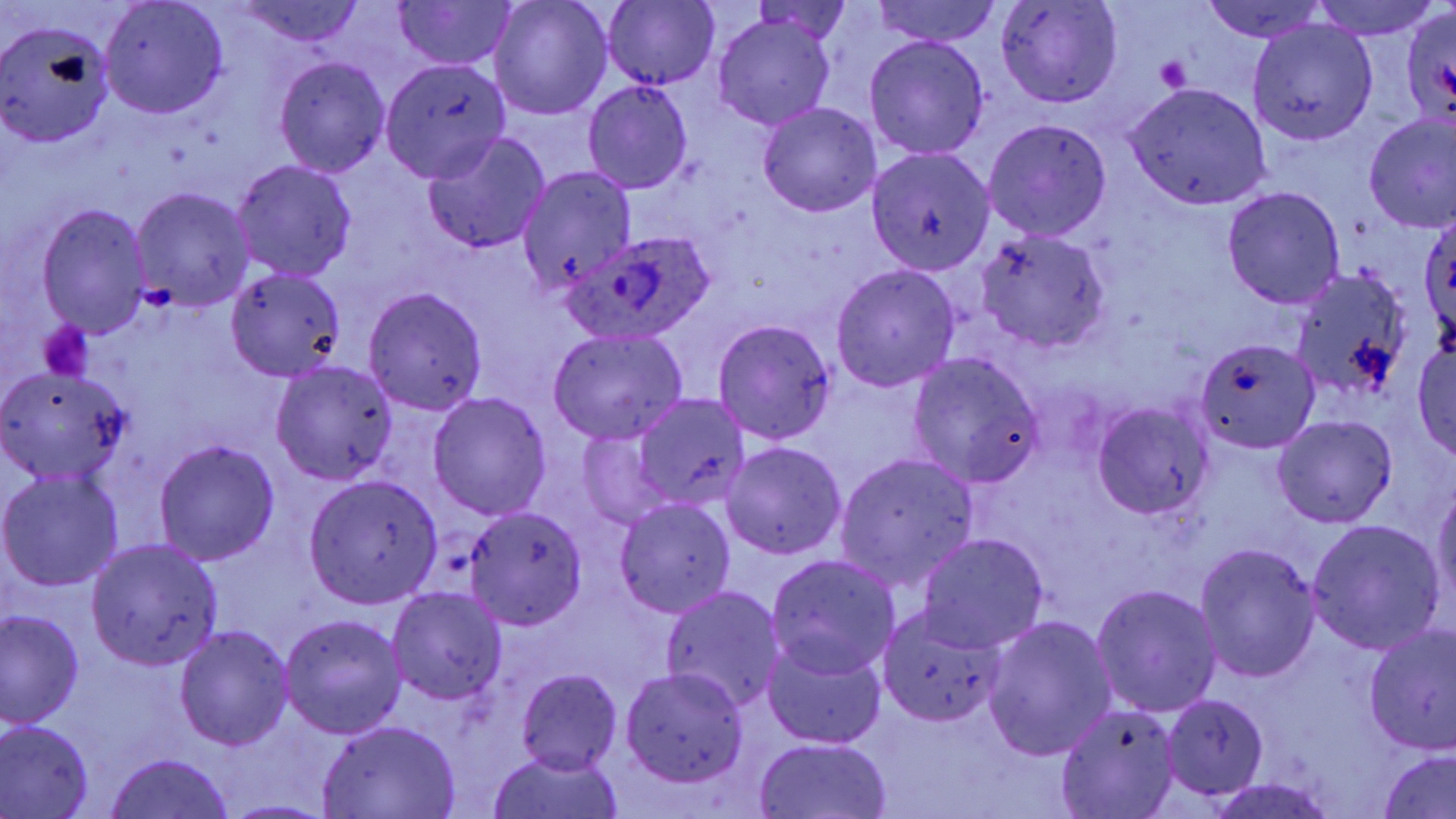

slide-level diagnosis = Plasmodium ovale
magnification = 1000x
image size = 1456×819 pixels
Plasmodium ovale-infected red blood cell locations = approximate bounding boxes as named x1/y1/x2/y2 corners in pixels: (x1=559, y1=232, x2=717, y2=345)
preparation = thin blood smear
uninfected red blood cell locations = approximate bounding boxes as named x1/y1/x2/y2 corners in pixels: (x1=100, y1=0, x2=229, y2=119), (x1=236, y1=0, x2=369, y2=48), (x1=391, y1=0, x2=516, y2=71), (x1=872, y1=0, x2=1003, y2=48), (x1=1203, y1=0, x2=1327, y2=42), (x1=1309, y1=0, x2=1441, y2=39), (x1=488, y1=1, x2=614, y2=120), (x1=749, y1=1, x2=856, y2=45), (x1=994, y1=1, x2=1124, y2=108), (x1=602, y1=2, x2=719, y2=89), (x1=1397, y1=9, x2=1456, y2=128), (x1=713, y1=14, x2=835, y2=130), (x1=0, y1=19, x2=114, y2=147), (x1=1248, y1=19, x2=1378, y2=144), (x1=864, y1=35, x2=990, y2=160), (x1=273, y1=55, x2=391, y2=177), (x1=379, y1=59, x2=513, y2=183), (x1=582, y1=79, x2=693, y2=194), (x1=1124, y1=83, x2=1270, y2=209), (x1=757, y1=102, x2=882, y2=217), (x1=1363, y1=113, x2=1456, y2=234), (x1=983, y1=118, x2=1112, y2=239), (x1=420, y1=132, x2=551, y2=255), (x1=866, y1=147, x2=997, y2=274), (x1=231, y1=159, x2=357, y2=282), (x1=518, y1=166, x2=637, y2=298), (x1=1221, y1=186, x2=1346, y2=309), (x1=130, y1=187, x2=255, y2=310), (x1=35, y1=203, x2=152, y2=338), (x1=1419, y1=208, x2=1456, y2=348), (x1=977, y1=231, x2=1112, y2=353), (x1=831, y1=264, x2=960, y2=392), (x1=225, y1=266, x2=348, y2=380), (x1=1289, y1=268, x2=1419, y2=407), (x1=362, y1=285, x2=490, y2=415), (x1=713, y1=320, x2=836, y2=444), (x1=549, y1=327, x2=688, y2=444), (x1=1194, y1=338, x2=1318, y2=452), (x1=1414, y1=339, x2=1455, y2=462), (x1=907, y1=353, x2=1044, y2=487), (x1=269, y1=361, x2=397, y2=485), (x1=0, y1=364, x2=134, y2=485), (x1=430, y1=392, x2=551, y2=519), (x1=633, y1=395, x2=750, y2=511), (x1=1093, y1=401, x2=1216, y2=520), (x1=1273, y1=415, x2=1396, y2=527), (x1=577, y1=430, x2=669, y2=529), (x1=155, y1=439, x2=279, y2=565), (x1=721, y1=441, x2=847, y2=560), (x1=835, y1=452, x2=978, y2=590), (x1=1, y1=470, x2=124, y2=592), (x1=304, y1=475, x2=443, y2=607), (x1=1431, y1=481, x2=1456, y2=618), (x1=615, y1=498, x2=736, y2=618), (x1=463, y1=506, x2=587, y2=629), (x1=1305, y1=519, x2=1445, y2=655), (x1=916, y1=534, x2=1050, y2=653), (x1=86, y1=538, x2=222, y2=670), (x1=1194, y1=543, x2=1321, y2=683), (x1=765, y1=554, x2=900, y2=681), (x1=1091, y1=583, x2=1222, y2=718), (x1=661, y1=585, x2=785, y2=712), (x1=387, y1=587, x2=508, y2=706), (x1=1, y1=610, x2=83, y2=728), (x1=877, y1=610, x2=1007, y2=730), (x1=278, y1=613, x2=407, y2=739), (x1=981, y1=615, x2=1116, y2=763), (x1=174, y1=626, x2=294, y2=751), (x1=1362, y1=626, x2=1456, y2=757), (x1=762, y1=638, x2=889, y2=751), (x1=619, y1=667, x2=751, y2=787), (x1=516, y1=668, x2=622, y2=775), (x1=1162, y1=694, x2=1267, y2=797), (x1=1055, y1=702, x2=1181, y2=818), (x1=0, y1=720, x2=95, y2=817), (x1=317, y1=720, x2=461, y2=818), (x1=754, y1=738, x2=893, y2=818), (x1=486, y1=748, x2=625, y2=819), (x1=1378, y1=749, x2=1456, y2=818), (x1=104, y1=752, x2=237, y2=819), (x1=1208, y1=778, x2=1338, y2=818), (x1=217, y1=798, x2=339, y2=817)
stain = May-Grünwald-Giemsa
platelet locations = approximate bounding boxes as named x1/y1/x2/y2 corners in pixels: (x1=1154, y1=55, x2=1190, y2=92), (x1=37, y1=321, x2=94, y2=380)
field of view = single
modality = light microscopy